Report the malaria status of this cell.
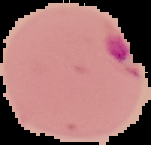

It is parasitized.

preparation = thin blood smear
image type = segmented cell region on a black background
image size = 151×145 pixels